Assess for malaria.
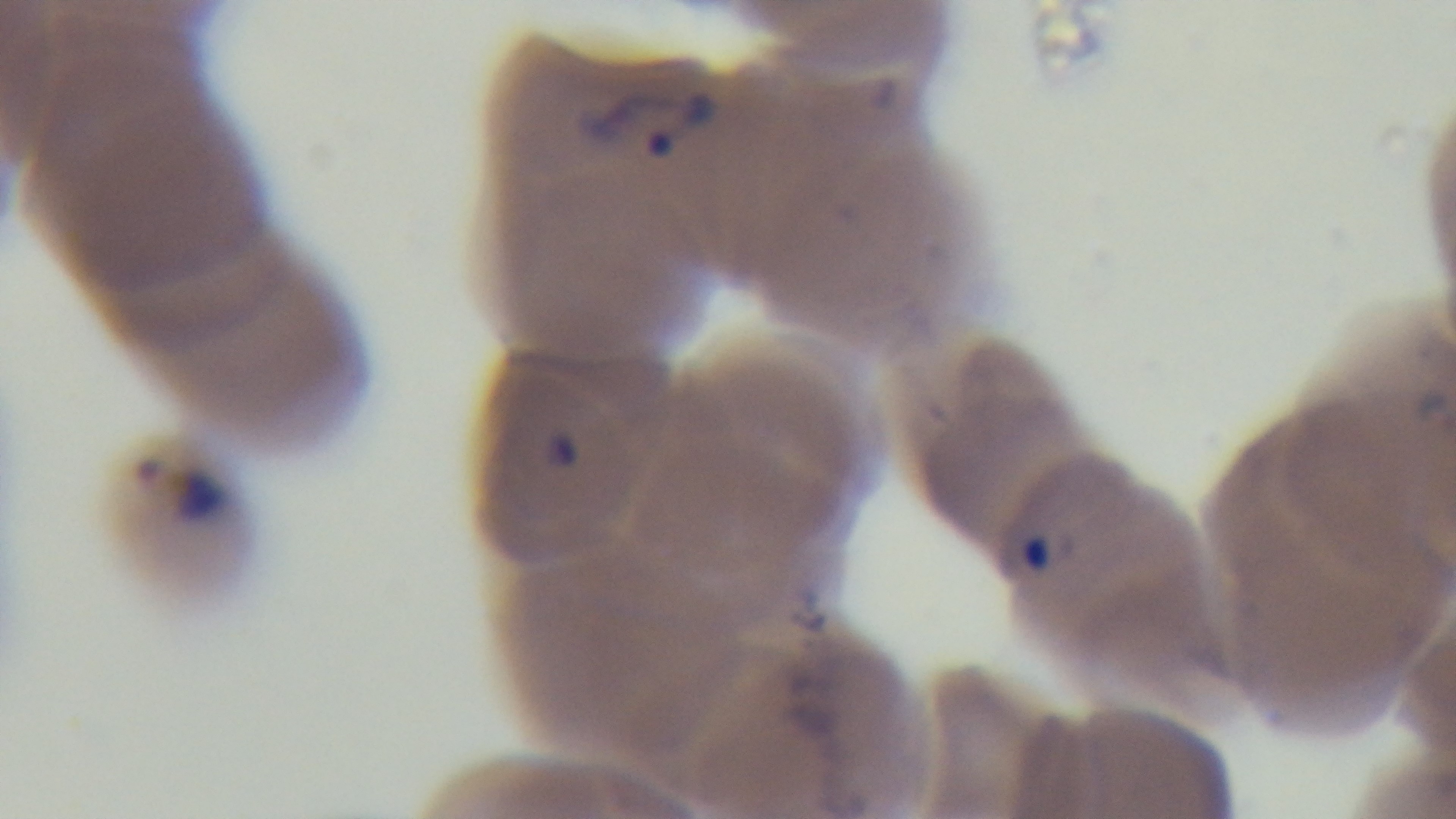

Infected.

field of view = single
stain = Giemsa
modality = light microscopy
capture = mounted 4K digital camera
preparation = thin
objective = 100x oil immersion